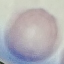

Summary:
  - Malaria status: uninfected
  - Capture: smartphone camera at the microscope eyepiece
  - Image type: automatically extracted cell patch, resized to 64 × 64 pixels
  - Preparation: thin blood smear
  - Stain: Giemsa